Comment on the morphology of the erythrocytes.
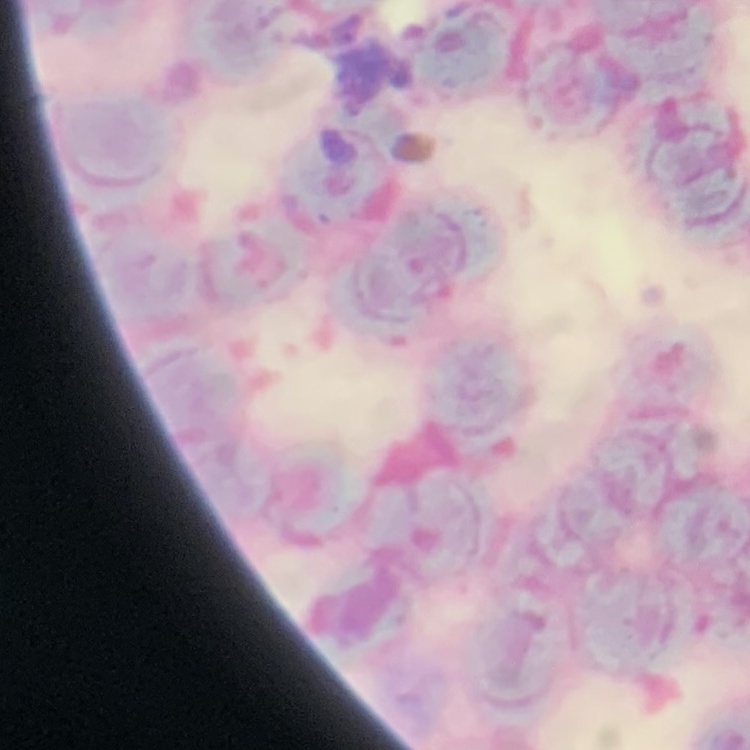

Rouleaux formation.

Summary:
  - Preparation: thin blood film
  - Stain: Field's or Giemsa
  - Image type: square crop of a larger photomicrograph